State the preparation type.
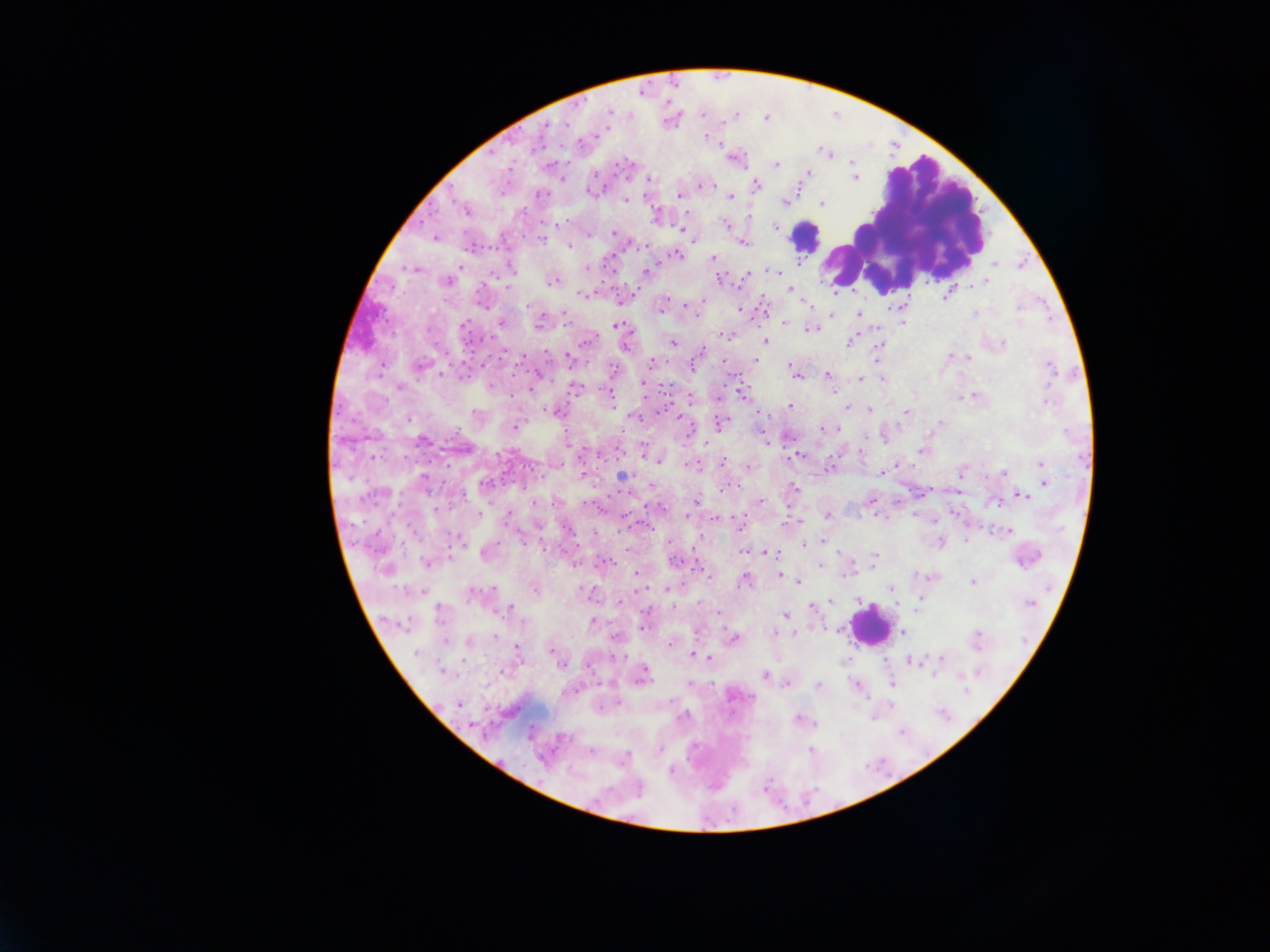
Thick blood film.

Approximate centers as [x, y] in pixels. Leukocyte locations: [914, 220], [867, 627]. Malaria parasite locations: [609, 113], [703, 116], [734, 117], [563, 125], [702, 137], [707, 139], [627, 162], [775, 164], [808, 173], [807, 176], [649, 178], [851, 179], [756, 184], [704, 185], [590, 195], [678, 196], [732, 197], [625, 202], [782, 202], [822, 204], [748, 217], [724, 225], [774, 227], [682, 229], [614, 233], [433, 237], [541, 239], [643, 242], [742, 244], [570, 246], [677, 254], [712, 258], [798, 263], [994, 266], [587, 268], [415, 270], [647, 271], [769, 271], [775, 271], [745, 275], [718, 277], [444, 281], [552, 282], [985, 282], [989, 282], [790, 291], [838, 293], [582, 295], [946, 296], [664, 297], [662, 303], [483, 305], [530, 305], [524, 306], [691, 306], [810, 306], [763, 309], [743, 310], [831, 314], [858, 314], [974, 314], [565, 316], [502, 323], [783, 324], [901, 324], [464, 326], [614, 326], [811, 329], [875, 330], [729, 335], [764, 340], [588, 341], [672, 344], [846, 344], [700, 350], [547, 352], [568, 356], [876, 358], [968, 359], [653, 361], [752, 361], [754, 363], [694, 364], [419, 365], [789, 366], [1049, 371], [794, 374], [732, 375], [829, 375], [441, 376], [538, 376], [797, 378], [860, 379], [882, 380], [644, 383], [399, 387], [531, 390], [609, 395], [741, 395], [612, 401], [1044, 402], [789, 405], [845, 408], [552, 410], [868, 410], [905, 413], [634, 417], [677, 418], [409, 419], [519, 422], [514, 424], [717, 426], [822, 429], [828, 429], [764, 436], [424, 442], [461, 450], [861, 451], [921, 451], [797, 457], [375, 458], [789, 458], [653, 460], [657, 462], [723, 463], [1041, 463], [746, 466], [884, 470], [1002, 474], [423, 476], [621, 476], [487, 482], [1044, 483], [732, 484], [793, 487], [1024, 495], [695, 501], [760, 501], [999, 501], [536, 503], [586, 503], [858, 513], [510, 516], [683, 516], [828, 516], [717, 520], [644, 525], [740, 526], [650, 527], [1012, 530], [458, 538], [524, 541], [805, 543], [965, 543], [742, 552], [768, 553], [778, 553], [873, 554], [608, 561], [678, 561], [875, 561], [427, 564], [574, 564], [1018, 565], [699, 566], [386, 568], [638, 573], [851, 573], [780, 575], [844, 575], [745, 579], [973, 582], [798, 583], [407, 589], [535, 589], [664, 589], [891, 589], [484, 591], [476, 593], [622, 598], [922, 600], [625, 601], [858, 601], [830, 602], [1029, 604], [670, 606], [512, 607], [648, 610], [812, 610], [716, 615], [783, 616], [591, 621], [642, 624], [524, 625], [641, 629], [900, 631], [774, 633], [796, 633], [977, 634], [613, 638], [496, 639], [734, 639], [447, 640], [468, 643], [671, 645], [518, 647], [548, 650], [693, 655], [700, 655], [620, 657], [710, 658], [941, 659], [911, 661], [843, 662], [907, 662], [465, 663], [561, 664], [644, 669], [442, 671], [503, 671], [646, 674], [765, 674], [934, 677], [644, 679], [785, 685], [894, 685], [818, 687], [459, 704], [618, 704], [890, 705], [685, 715], [796, 720], [660, 749], [590, 750], [670, 771]. Image is 1270×952 pixels. Single field of view. Collected in Ghana. Mobile-phone photograph taken through the microscope.